Classify this cell by malaria status.
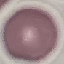

It is uninfected.

capture = smartphone camera at the microscope eyepiece
stain = Giemsa
preparation = thin blood film
image type = cell patch, automatically extracted from a larger field of view and resized to 64 × 64 pixels